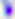

Summary:
  - Magnification: 400x
  - Modality: photomicrograph
  - Identification: Toxoplasma gondii